Assess this cell for malaria.
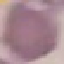
It is uninfected.

stain = Giemsa
image type = cell patch, automatically extracted from a larger field of view and resized to 64 × 64 pixels
capture = smartphone camera at the microscope eyepiece
preparation = thin blood film